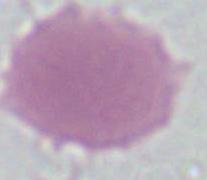
{
  "modality": "photomicrograph",
  "identification": "erythrocyte",
  "magnification": "1000x"
}